Classify the preparation.
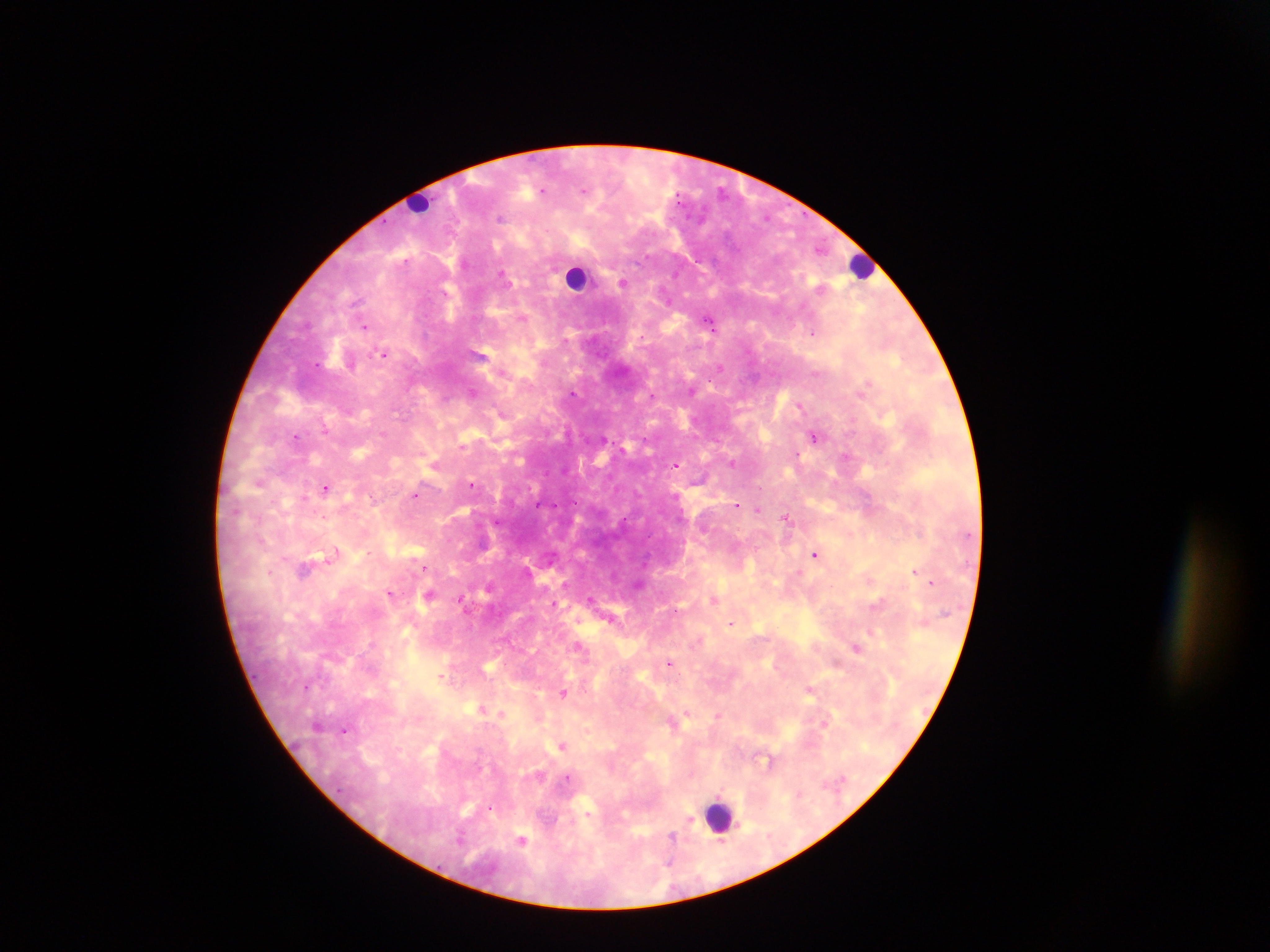

Thick blood film.

capture = mobile-phone photograph through a microscope
leukocyte locations = approximate centers as {x, y} in pixels: {419, 202}, {862, 266}, {577, 277}, {719, 815}
image size = 1270×952 pixels
Plasmodium parasite locations = approximate centers as {x, y} in pixels: {542, 190}, {584, 190}, {500, 218}, {405, 260}, {501, 274}, {623, 282}, {357, 301}, {522, 317}, {710, 324}, {365, 326}, {813, 332}, {384, 354}, {316, 364}, {720, 367}, {472, 392}, {573, 392}, {861, 392}, {652, 395}, {800, 405}, {324, 430}, {296, 436}, {813, 436}, {845, 456}, {676, 466}, {259, 482}, {471, 485}, {326, 487}, {414, 495}, {304, 497}, {537, 505}, {737, 505}, {758, 510}, {786, 517}, {816, 554}, {332, 555}, {423, 568}, {303, 570}, {799, 571}, {914, 571}, {931, 583}, {488, 586}, {390, 593}, {429, 595}, {460, 598}, {590, 599}, {715, 599}, {554, 604}, {877, 604}, {610, 619}, {731, 623}, {579, 646}, {857, 647}, {670, 662}, {442, 677}, {810, 690}, {563, 693}, {481, 709}, {687, 712}, {501, 714}, {718, 715}, {825, 724}, {344, 729}, {562, 746}, {568, 777}, {490, 808}, {689, 821}, {671, 837}, {460, 838}, {521, 841}, {722, 841}
field of view = single
country = Ghana